Classify this cell by malaria status.
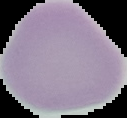
Uninfected.

Summary:
  - Image type: segmented cell region on a black background
  - Preparation: thin blood smear
  - Image size: 127×118 pixels